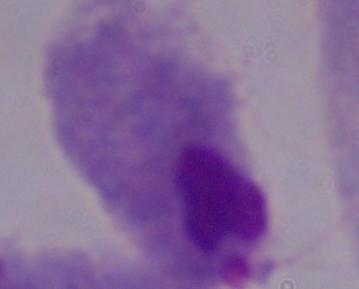

magnification = 1000x
modality = photomicrograph
identification = trichomonad